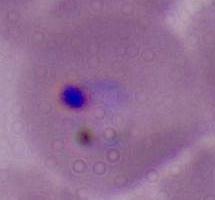 400x or 1000x magnification. Photomicrograph. A Plasmodium parasite is shown.